Report the malaria status of this cell.
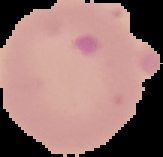
Uninfected.

The area outside the segmented cell region is set to black. Image is 163×157 pixels. From a thin blood smear.